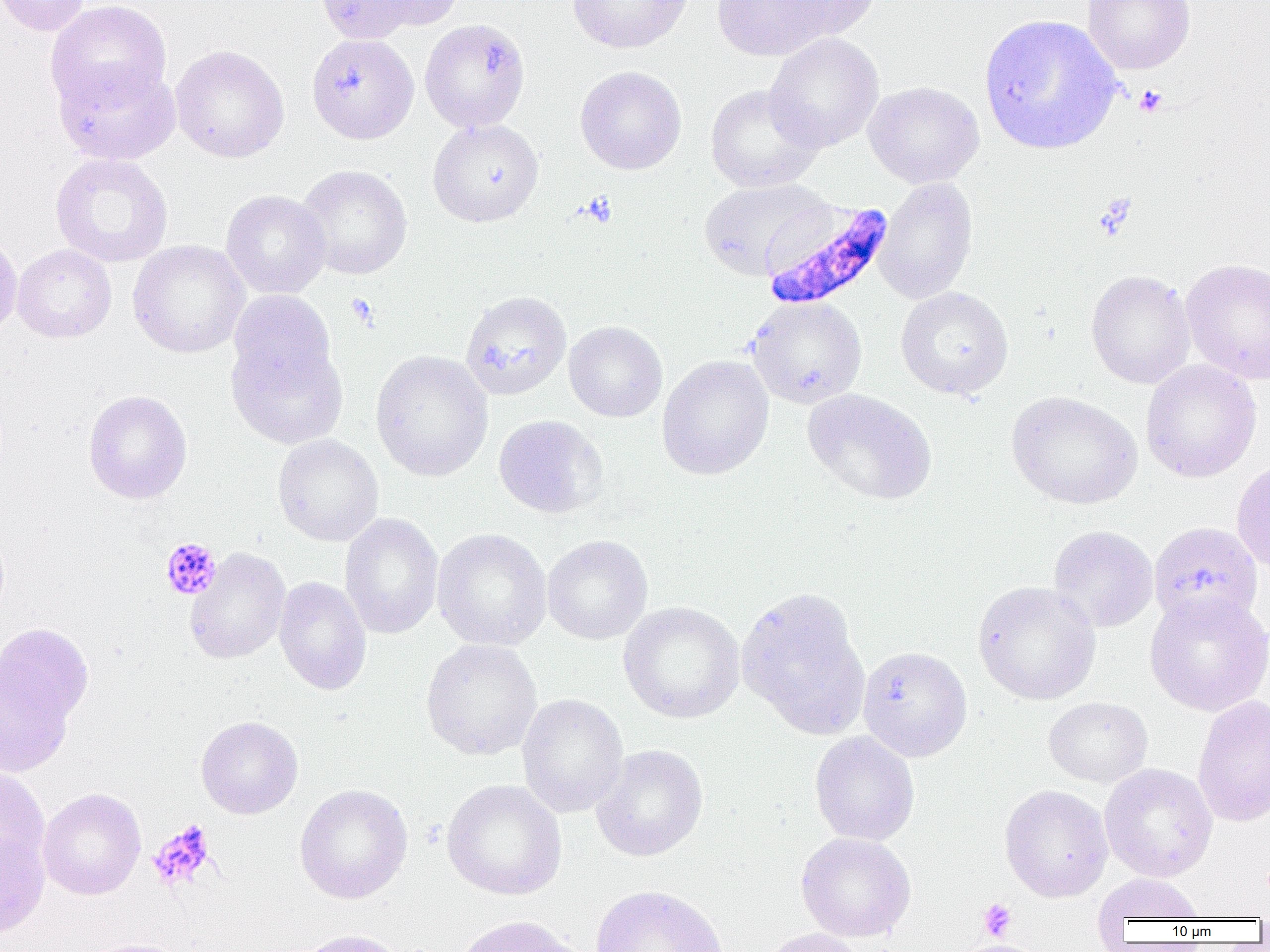
Summary:
  - Coordinate format: approximate bounding boxes as [x1, y1, x2, y2] in pixels
  - Plasmodium falciparum-infected red blood cell locations: [761, 201, 896, 312]
  - Uninfected red blood cell locations: [1, 0, 91, 36], [45, 0, 172, 113], [314, 0, 422, 45], [361, 0, 464, 31], [567, 0, 693, 54], [712, 0, 842, 61], [771, 0, 882, 41], [1081, 0, 1196, 75], [979, 13, 1123, 155], [420, 18, 530, 133], [764, 32, 884, 153], [306, 33, 419, 144], [170, 45, 290, 162], [53, 59, 181, 165], [574, 66, 687, 175], [863, 81, 984, 188], [704, 84, 824, 193], [427, 118, 544, 227], [49, 153, 173, 268], [295, 164, 413, 280], [698, 177, 832, 280], [874, 177, 978, 305], [221, 190, 331, 299], [0, 231, 22, 341], [128, 240, 250, 358], [11, 244, 117, 343], [1180, 257, 1270, 384], [1085, 269, 1196, 389], [895, 286, 1014, 400], [460, 290, 572, 400], [226, 291, 338, 395], [746, 296, 867, 408], [564, 320, 667, 422], [226, 333, 349, 450], [370, 349, 493, 482], [656, 354, 774, 480], [1140, 359, 1262, 483], [801, 388, 938, 506], [82, 389, 193, 504], [1006, 390, 1142, 510], [493, 414, 607, 518], [272, 434, 383, 546], [1232, 459, 1270, 574], [340, 512, 444, 640], [1149, 521, 1264, 628], [1048, 525, 1158, 632], [431, 528, 552, 651], [542, 535, 652, 644], [185, 548, 291, 664], [274, 576, 372, 696], [972, 580, 1101, 705], [736, 587, 871, 739], [1144, 590, 1269, 716], [618, 601, 745, 724], [0, 623, 94, 744], [421, 638, 543, 761], [857, 646, 973, 761], [516, 693, 629, 818], [1192, 694, 1270, 828], [1044, 696, 1153, 788], [195, 716, 303, 819], [809, 731, 920, 846], [591, 744, 708, 862], [1099, 763, 1218, 881], [0, 767, 49, 874], [441, 779, 567, 900], [294, 783, 413, 904], [999, 784, 1113, 902], [37, 788, 146, 900], [0, 827, 49, 938], [795, 832, 916, 942], [1092, 873, 1205, 924], [590, 884, 729, 952], [451, 915, 586, 952], [757, 927, 867, 952], [292, 928, 408, 952], [82, 939, 189, 952], [956, 939, 1047, 952]
  - Platelet locations: [1134, 85, 1167, 117], [580, 192, 617, 228], [345, 293, 379, 328], [160, 536, 221, 600], [147, 821, 216, 891], [978, 898, 1016, 941]
  - Slide-level diagnosis: Plasmodium falciparum
  - Preparation: thin blood film
  - Magnification: 1000x
  - Modality: optical microscopy
  - Field of view: single
  - Image size: 1270×952 pixels